Locate and identify every blood parasite.
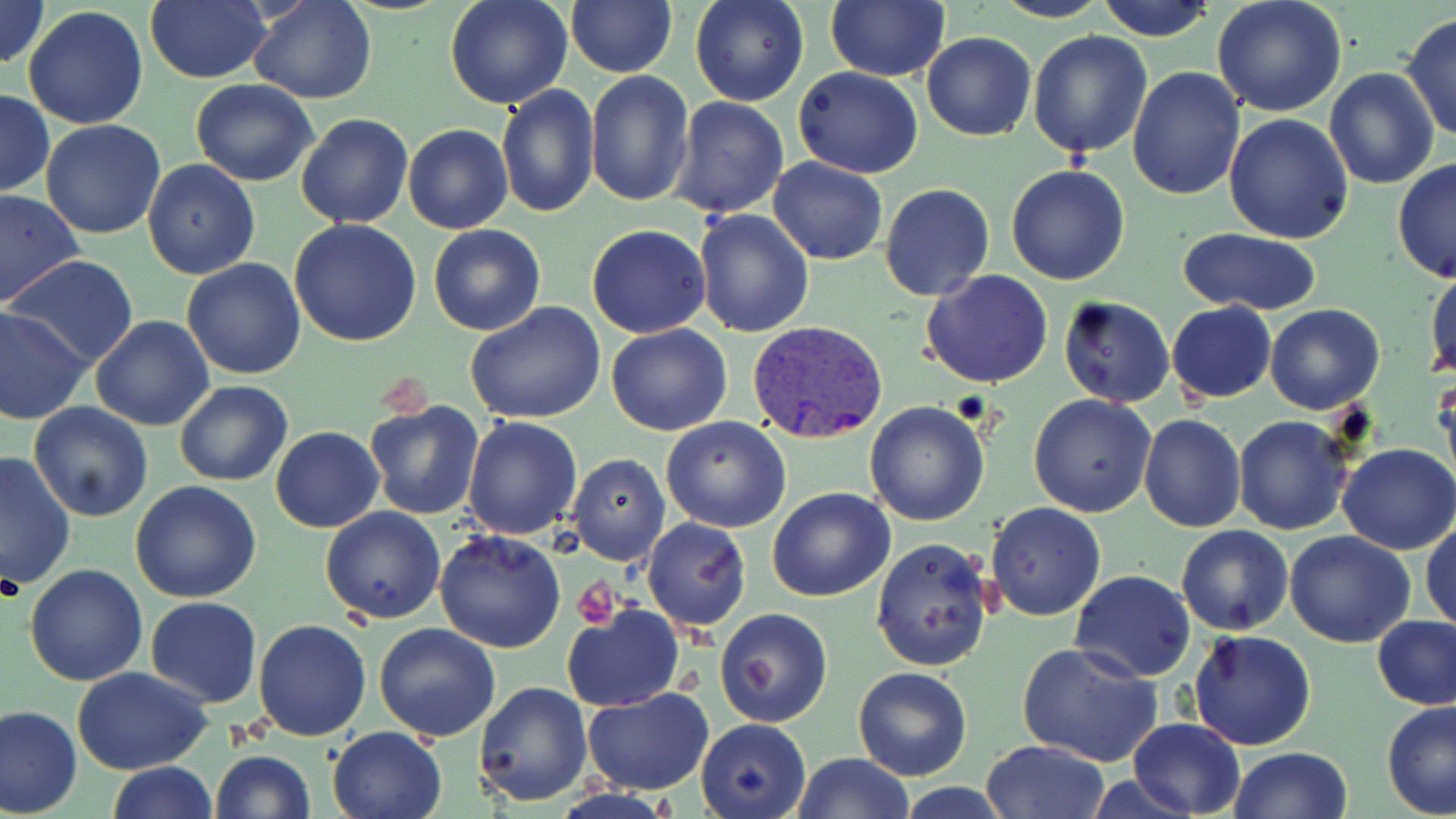
Approximate bounding boxes as [x1, y1, x2, y2] in pixels.
Plasmodium vivax-infected red blood cells: [746, 320, 889, 446].
No Plasmodium falciparum, Plasmodium ovale, Plasmodium malariae, Babesia divergens, or Trypanosoma brucei observed.

Summary:
  - Uninfected red blood cell locations: [0, 0, 48, 71], [145, 0, 271, 84], [248, 0, 378, 104], [444, 0, 574, 110], [566, 0, 677, 78], [689, 0, 811, 107], [825, 0, 949, 82], [992, 0, 1111, 23], [1096, 0, 1216, 42], [1211, 2, 1348, 118], [23, 6, 150, 130], [1400, 12, 1456, 145], [1026, 31, 1152, 160], [921, 32, 1035, 141], [793, 66, 923, 178], [1324, 68, 1438, 189], [1127, 69, 1246, 201], [585, 71, 694, 207], [190, 79, 320, 186], [495, 83, 599, 219], [0, 89, 53, 198], [669, 96, 788, 219], [296, 113, 415, 228], [1223, 113, 1354, 246], [41, 119, 167, 238], [403, 123, 514, 234], [142, 158, 261, 280], [769, 158, 888, 266], [1392, 158, 1455, 283], [1005, 164, 1130, 285], [879, 182, 996, 301], [0, 189, 84, 310], [692, 210, 813, 338], [289, 220, 422, 348], [427, 224, 545, 336], [586, 224, 711, 339], [1176, 228, 1323, 315], [6, 256, 140, 370], [181, 258, 306, 380], [1426, 266, 1456, 380], [921, 270, 1055, 389], [1057, 296, 1176, 407], [1166, 301, 1276, 405], [463, 303, 608, 425], [1264, 304, 1385, 414], [0, 306, 92, 426], [91, 315, 215, 433], [605, 322, 732, 436], [1432, 366, 1455, 485], [174, 379, 292, 488], [1028, 394, 1157, 517], [366, 399, 486, 520], [28, 401, 153, 523], [864, 401, 990, 526], [1138, 414, 1246, 533], [460, 415, 582, 539], [1234, 415, 1355, 535], [660, 416, 791, 532], [270, 426, 384, 532], [1336, 442, 1455, 554], [0, 451, 75, 592], [568, 453, 672, 567], [131, 481, 262, 603], [767, 487, 895, 602], [987, 502, 1107, 620], [321, 506, 447, 623], [641, 517, 750, 632], [1421, 517, 1455, 634], [1175, 525, 1293, 635], [434, 531, 566, 653], [1285, 531, 1416, 648], [870, 537, 995, 672], [24, 563, 148, 685], [1068, 569, 1197, 682], [146, 597, 263, 707], [560, 602, 684, 713], [715, 608, 834, 728], [1373, 615, 1456, 709], [253, 618, 371, 742], [373, 621, 501, 742], [1188, 629, 1316, 750], [1017, 641, 1166, 769], [854, 666, 972, 781], [72, 667, 213, 776], [473, 680, 595, 807], [583, 689, 713, 795], [1381, 702, 1456, 818], [0, 705, 81, 818], [696, 718, 811, 818], [1128, 718, 1247, 818], [327, 726, 445, 819], [982, 740, 1108, 819], [1228, 748, 1350, 819], [208, 750, 316, 819], [793, 752, 912, 819], [105, 760, 215, 818], [898, 784, 1012, 817]
  - Platelet locations: [571, 582, 619, 629]
  - Slide-level diagnosis: Plasmodium vivax
  - Magnification: 1000x
  - Stain: May-Grünwald-Giemsa
  - Preparation: thin blood smear
  - Image size: 1456×819 pixels
  - Modality: optical microscopy
  - Field of view: one of a larger specimen